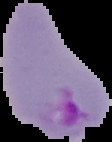

{
  "image_type": "segmented cell region with the area outside set to black",
  "image_size": "112×142 pixels",
  "malaria_status": "parasitized",
  "preparation": "thin blood film"
}